Classify this cell by malaria status.
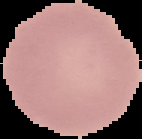
It is uninfected.

Segmented cell region on a black background. Image is 142×139 pixels. From a thin blood film.